Comment on the morphology of the erythrocytes.
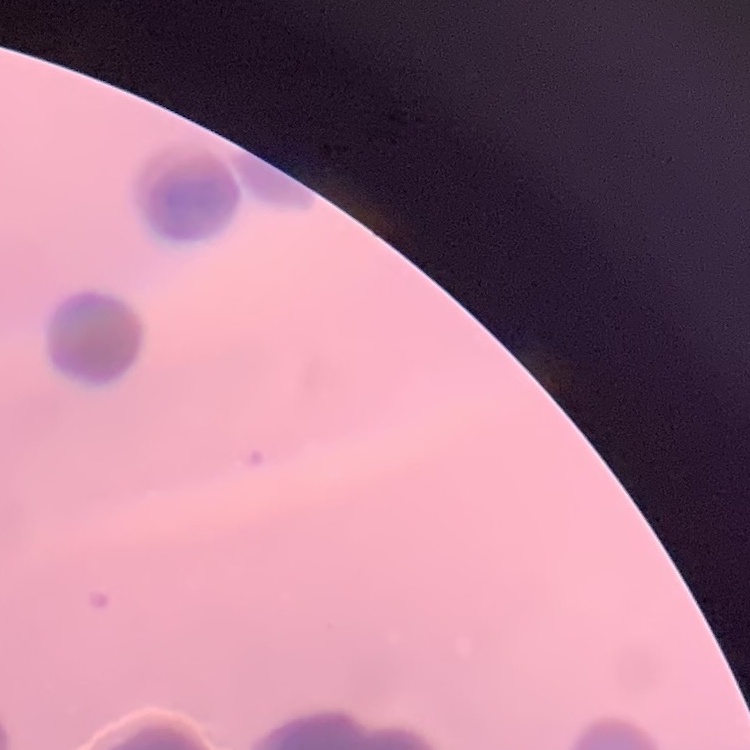
Rouleaux formation.

stain: Field's or Giemsa
preparation: thin blood smear
image_type: one tile cut from a larger photomicrograph